Identify the parasite.
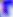
This is Toxoplasma gondii.

modality = micrograph
magnification = 400x